Assess the morphology of the erythrocytes.
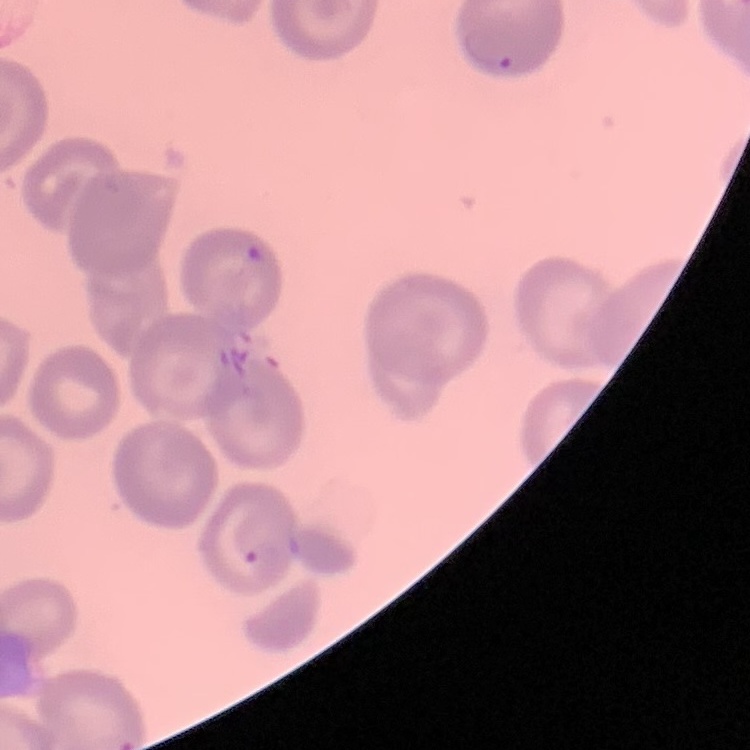

They show no rouleaux formation.

Field's or Giemsa stain. Square crop of a larger photomicrograph. Thin blood film.